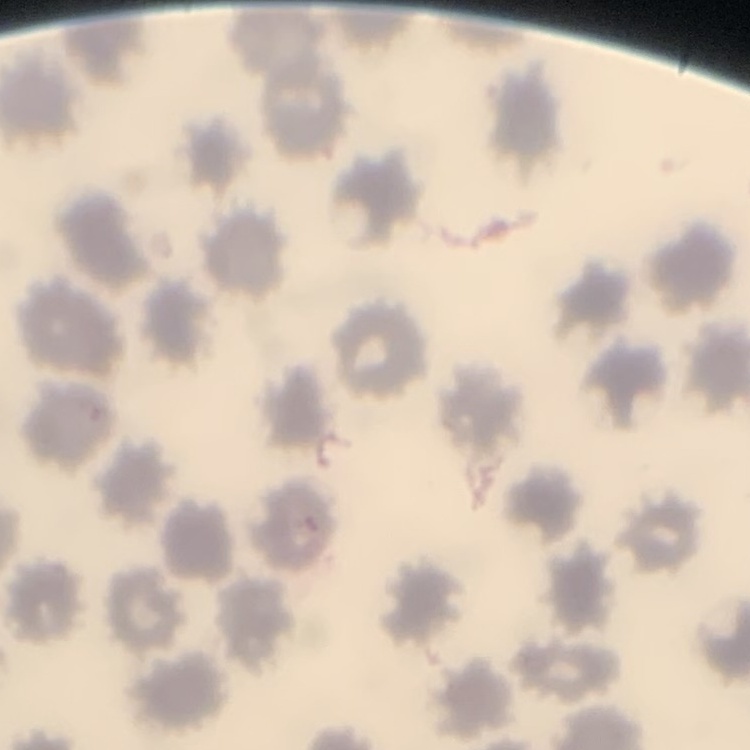
red blood cell morphology = no rouleaux formation
preparation = thin peripheral smear
image type = one tile cut from a larger photomicrograph
stain = Field's or Giemsa